Look for Plasmodium parasites.
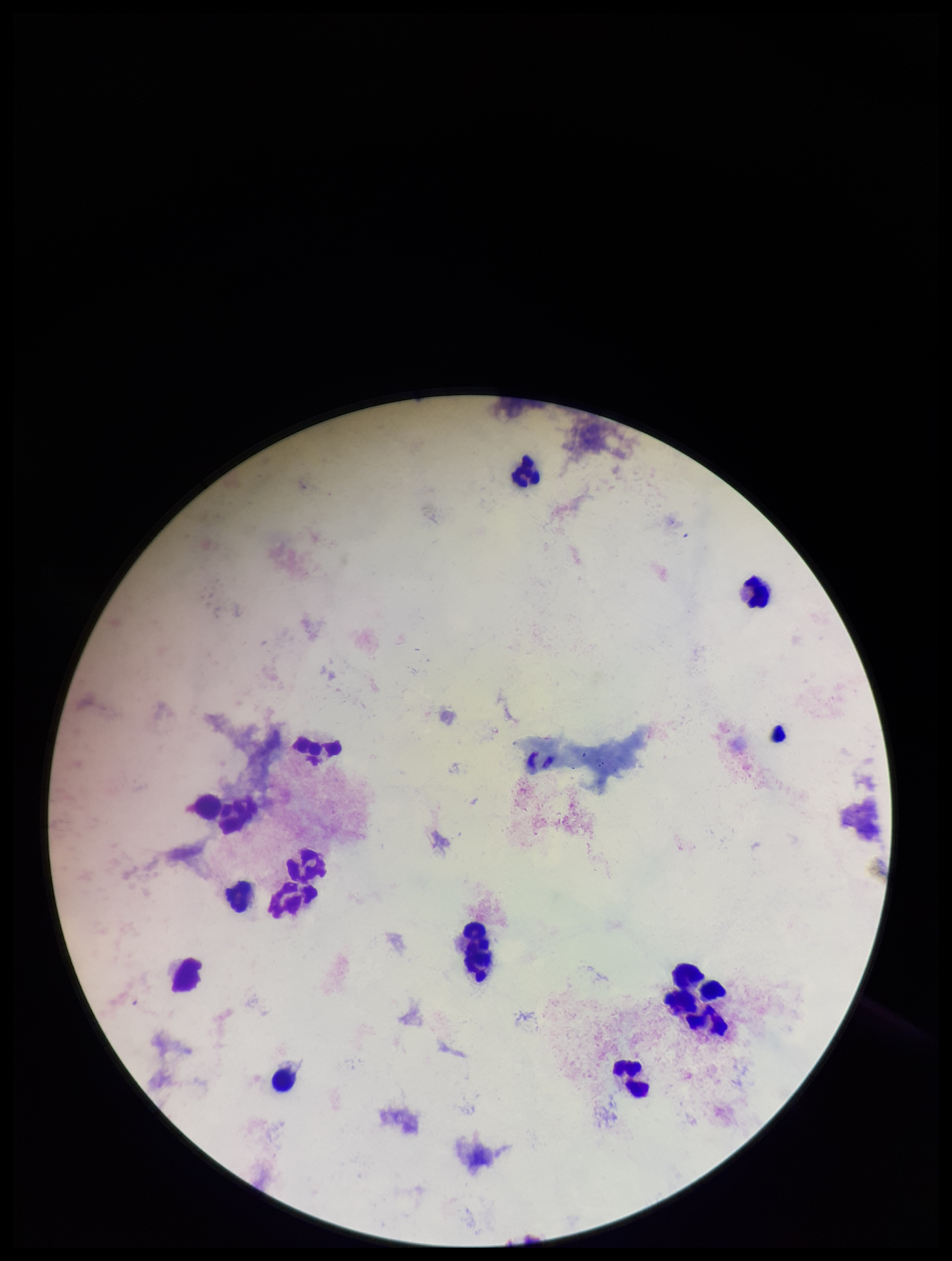

None detected.

Summary:
  - Stain: Giemsa
  - Preparation: thick blood smear
  - Leukocyte count: 14
  - Field of view: one from this slide
  - Patient malaria status: negative
  - Capture: smartphone photograph through the microscope eyepiece
  - Parasite count: 0
  - Image size: 952×1261 pixels